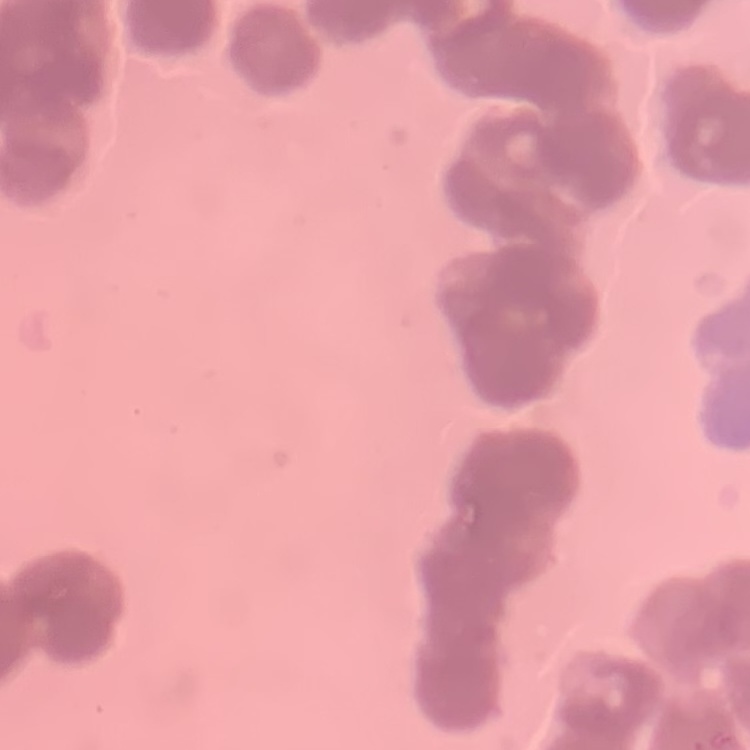
red blood cell morphology = rouleaux formation
image type = square crop of a larger photomicrograph
preparation = thin blood smear
stain = Field's or Giemsa